State the preparation type.
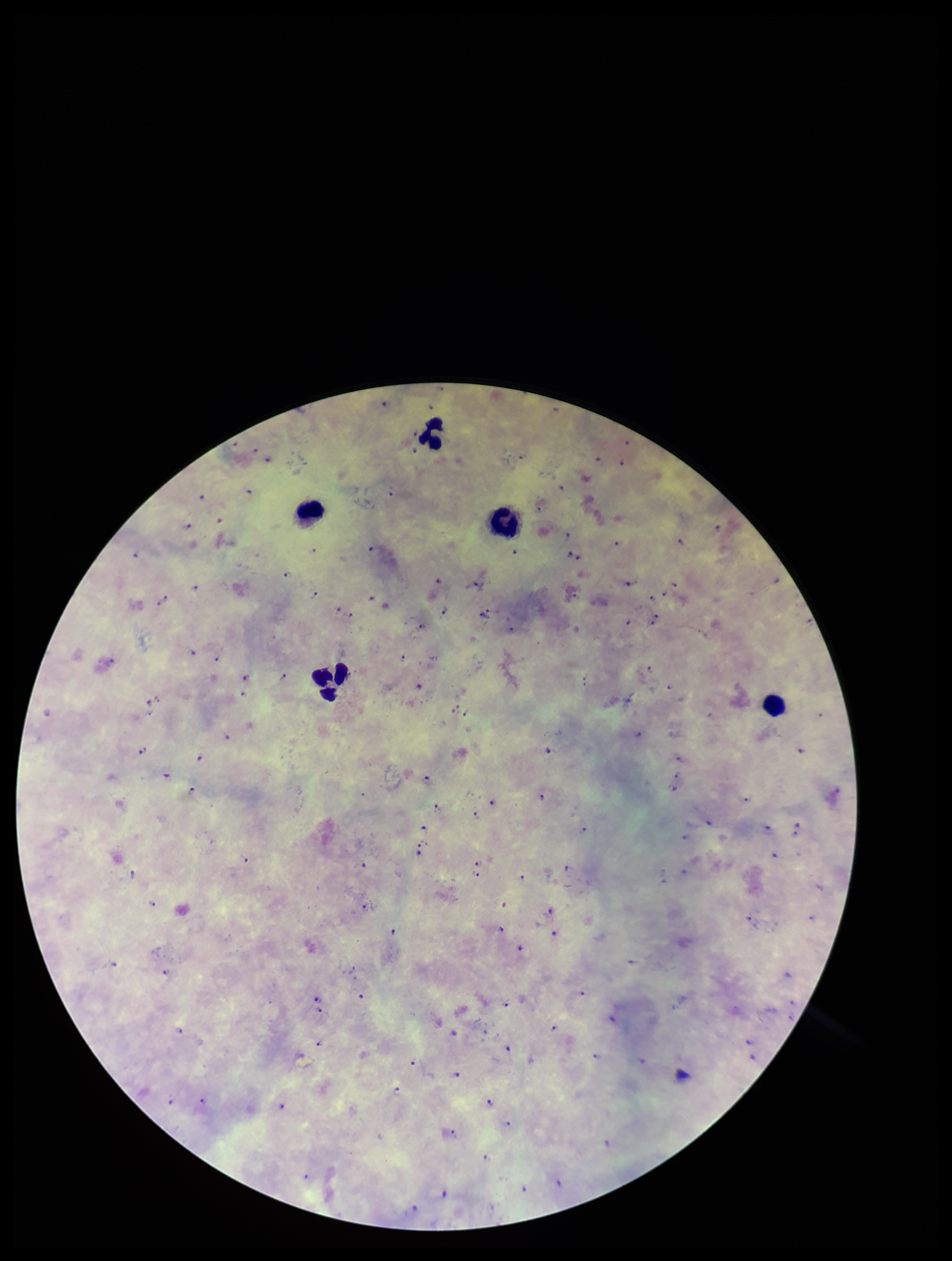
Thick.

Summary:
  - Parasite count: 99
  - Image size: 952×1261 pixels
  - Species reported for this patient: Plasmodium falciparum
  - Leukocyte count: 5
  - Capture: smartphone photograph through the microscope eyepiece
  - Plasmodium parasites: detected
  - Stain: Giemsa
  - Patient malaria status: infected
  - Field of view: single